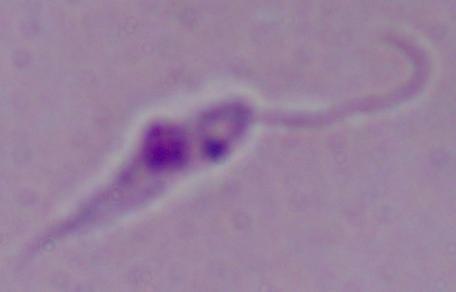
identification = Leishmania
modality = photomicrograph
magnification = 1000x